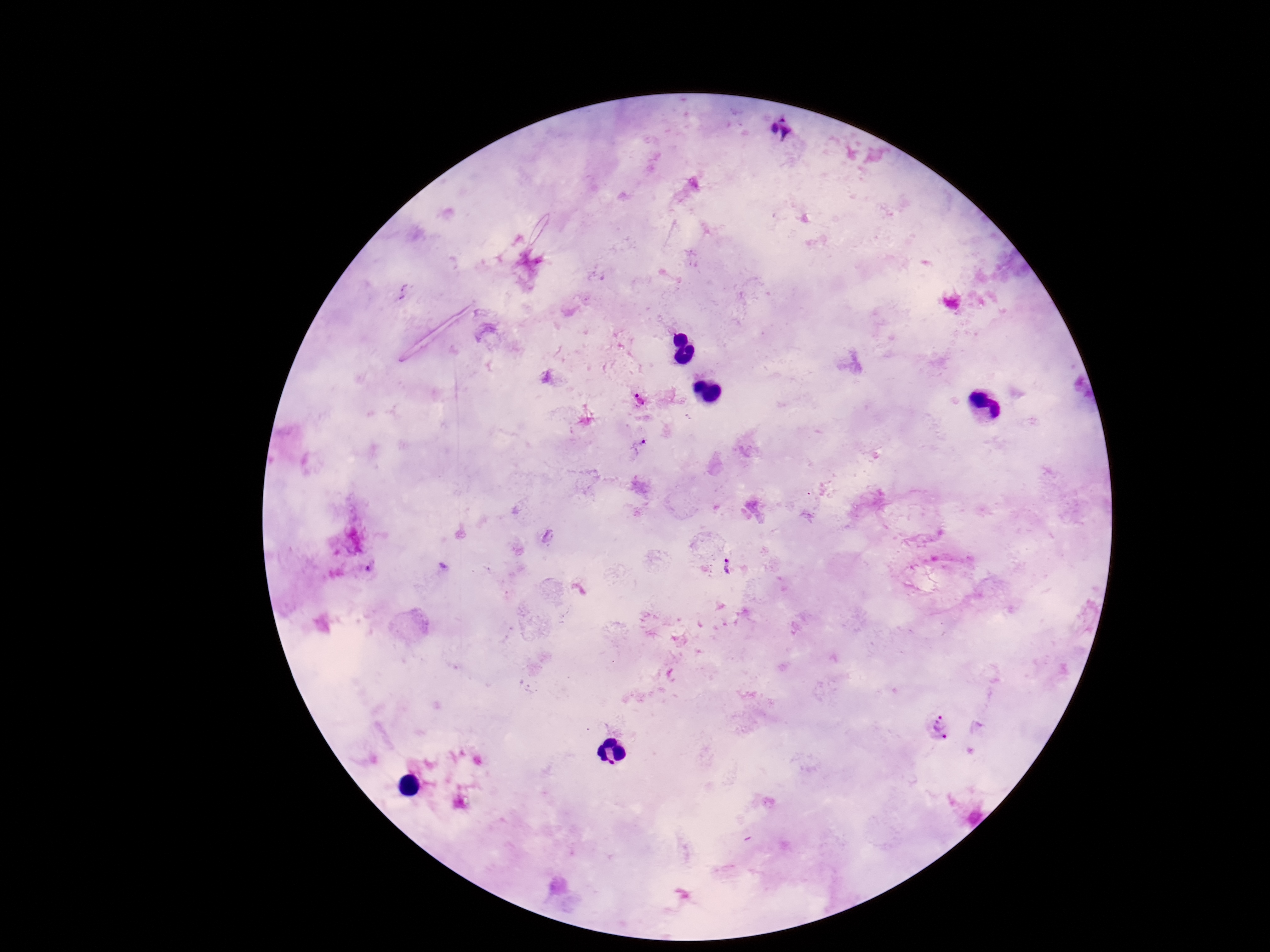

image size = 1270×952 pixels
magnification = 100x
Plasmodium parasite locations = approximate centers as (x, y) in pixels: (780, 128), (640, 400), (637, 445), (369, 566), (727, 566), (942, 727)
stain = Giemsa
preparation = thick blood film
field of view = one from this slide
capture = smartphone camera through the microscope eyepiece
patient malaria status = infected